Give the preparation type.
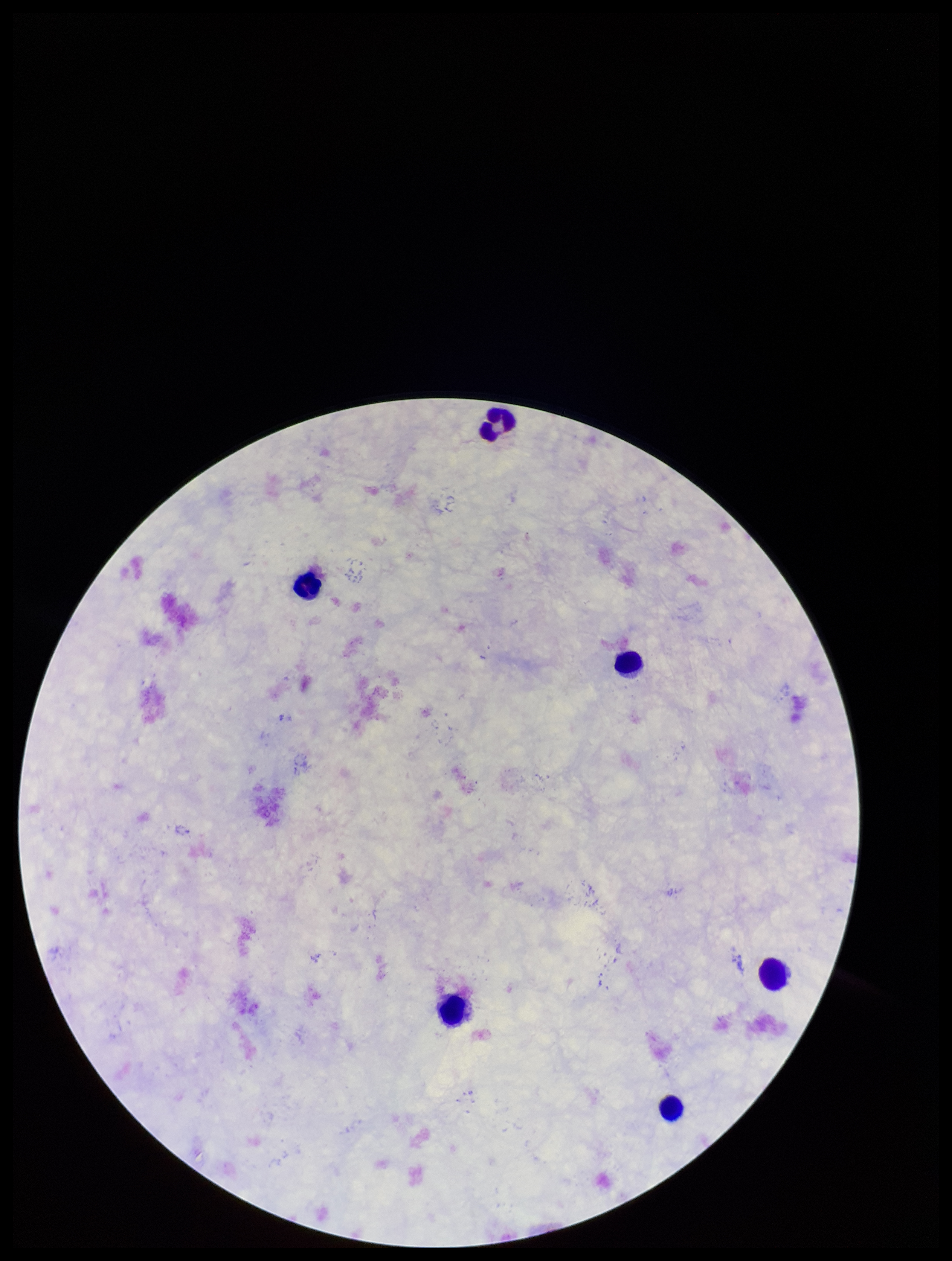
A thick smear.

Single field of view. Photographed through the microscope eyepiece with a smartphone camera. Plasmodium parasites: none detected. Parasite count: 0. Stained with Giemsa. Image is 952×1261 pixels. Patient malaria status: negative. Leukocyte count: 6.